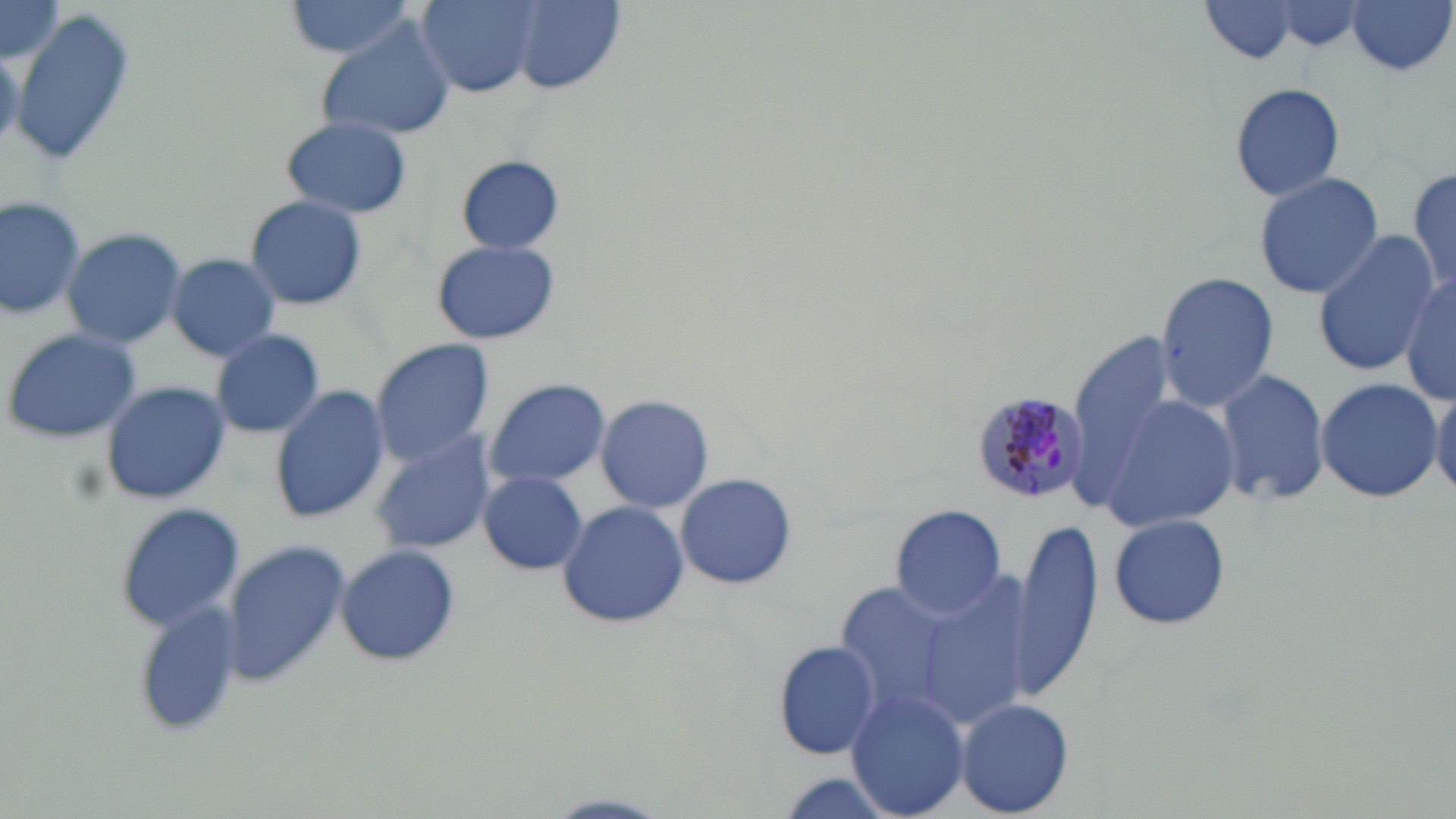
Summary:
  - Coordinate format: approximate bounding boxes as (x1, y1, x2, y2) in pixels
  - Uninfected red blood cell locations: (284, 0, 419, 61), (415, 0, 542, 98), (1195, 0, 1313, 67), (1346, 0, 1455, 77), (0, 1, 62, 62), (1262, 1, 1371, 53), (512, 2, 623, 93), (6, 12, 139, 168), (318, 22, 453, 144), (1228, 82, 1347, 203), (280, 115, 411, 219), (458, 156, 564, 254), (1407, 166, 1456, 303), (1252, 170, 1386, 301), (0, 193, 84, 317), (243, 195, 368, 311), (62, 227, 188, 350), (1315, 230, 1439, 378), (431, 239, 559, 345), (165, 253, 282, 362), (1155, 271, 1278, 412), (1400, 271, 1456, 409), (4, 326, 143, 445), (210, 328, 325, 439), (1065, 332, 1176, 518), (368, 339, 495, 464), (1216, 366, 1330, 508), (482, 377, 610, 490), (1312, 378, 1442, 502), (100, 381, 229, 505), (1430, 383, 1456, 497), (269, 385, 390, 524), (1098, 393, 1241, 534), (594, 395, 715, 513), (370, 434, 495, 556), (479, 471, 589, 576), (675, 471, 798, 590), (556, 500, 689, 630), (889, 503, 1009, 619), (113, 504, 245, 632), (1107, 511, 1232, 632), (1010, 517, 1103, 705), (221, 542, 350, 685), (336, 544, 459, 667), (833, 581, 958, 717), (919, 581, 1032, 728), (133, 606, 245, 738), (770, 640, 881, 761), (846, 685, 971, 818), (955, 697, 1075, 816)
  - Plasmodium malariae-infected red blood cell locations: (968, 391, 1087, 507)
  - Slide-level diagnosis: Plasmodium malariae
  - Modality: light microscopy
  - Magnification: 1000x
  - Field of view: one of a larger specimen
  - Preparation: thin blood smear
  - Stain: May-Grünwald-Giemsa
  - Image size: 1456×819 pixels